State the blood parasite species.
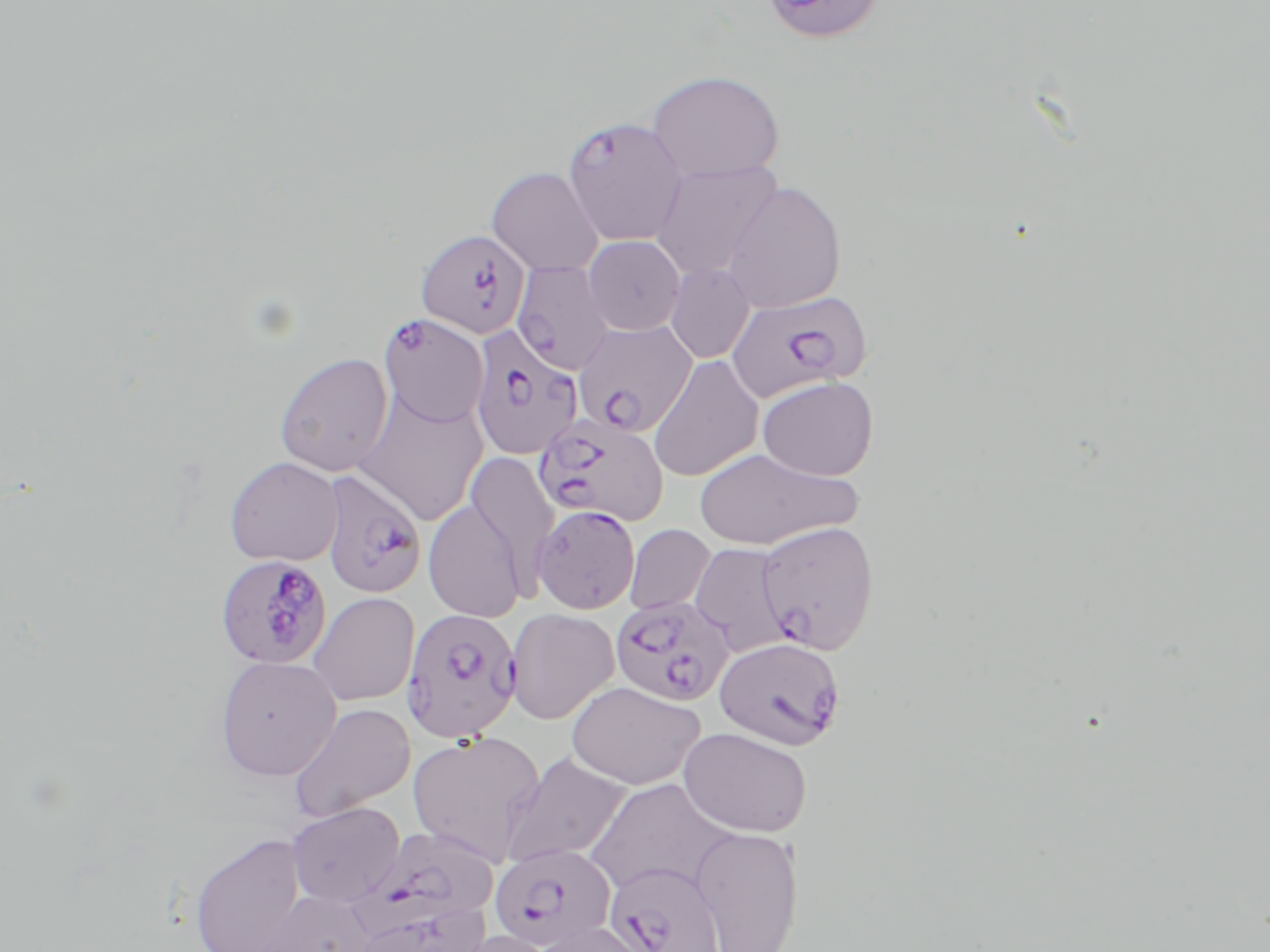

Plasmodium falciparum.

Approximate bounding boxes as (x1, y1, x2, y2) in pixels. Plasmodium falciparum-infected red blood cell locations: (561, 115, 689, 246), (415, 227, 531, 338), (510, 261, 615, 375), (726, 289, 871, 402), (378, 314, 489, 428), (573, 319, 697, 436), (468, 326, 584, 460), (533, 413, 668, 527), (321, 471, 428, 598), (532, 504, 640, 614), (755, 520, 880, 655), (215, 554, 333, 669), (610, 595, 735, 707), (400, 608, 523, 742), (714, 636, 845, 750), (357, 825, 500, 938), (489, 843, 617, 951), (603, 860, 726, 952). Uninfected red blood cell locations: (758, 0, 885, 44), (646, 70, 785, 183), (651, 160, 784, 280), (486, 167, 604, 276), (722, 181, 847, 313), (583, 235, 685, 335), (665, 263, 755, 363), (274, 351, 395, 477), (647, 354, 764, 482), (757, 375, 879, 480), (352, 389, 488, 526), (693, 447, 860, 551), (465, 451, 560, 583), (225, 456, 343, 566), (423, 498, 529, 621), (625, 524, 715, 616), (689, 542, 793, 656), (307, 592, 420, 706), (505, 608, 619, 725), (215, 655, 341, 780), (566, 681, 705, 790), (288, 702, 417, 822), (678, 726, 812, 838), (407, 730, 547, 865), (502, 751, 632, 867), (585, 778, 734, 898), (287, 802, 405, 907), (689, 825, 804, 952), (189, 830, 307, 952), (252, 887, 379, 952), (351, 900, 489, 952), (527, 920, 656, 952), (444, 929, 558, 952). May-Grünwald-Giemsa stain. Thin blood film. Image is 1270×952 pixels. One field of a larger specimen. Light microscopy. 1000x magnification.